Locate and identify every blood parasite.
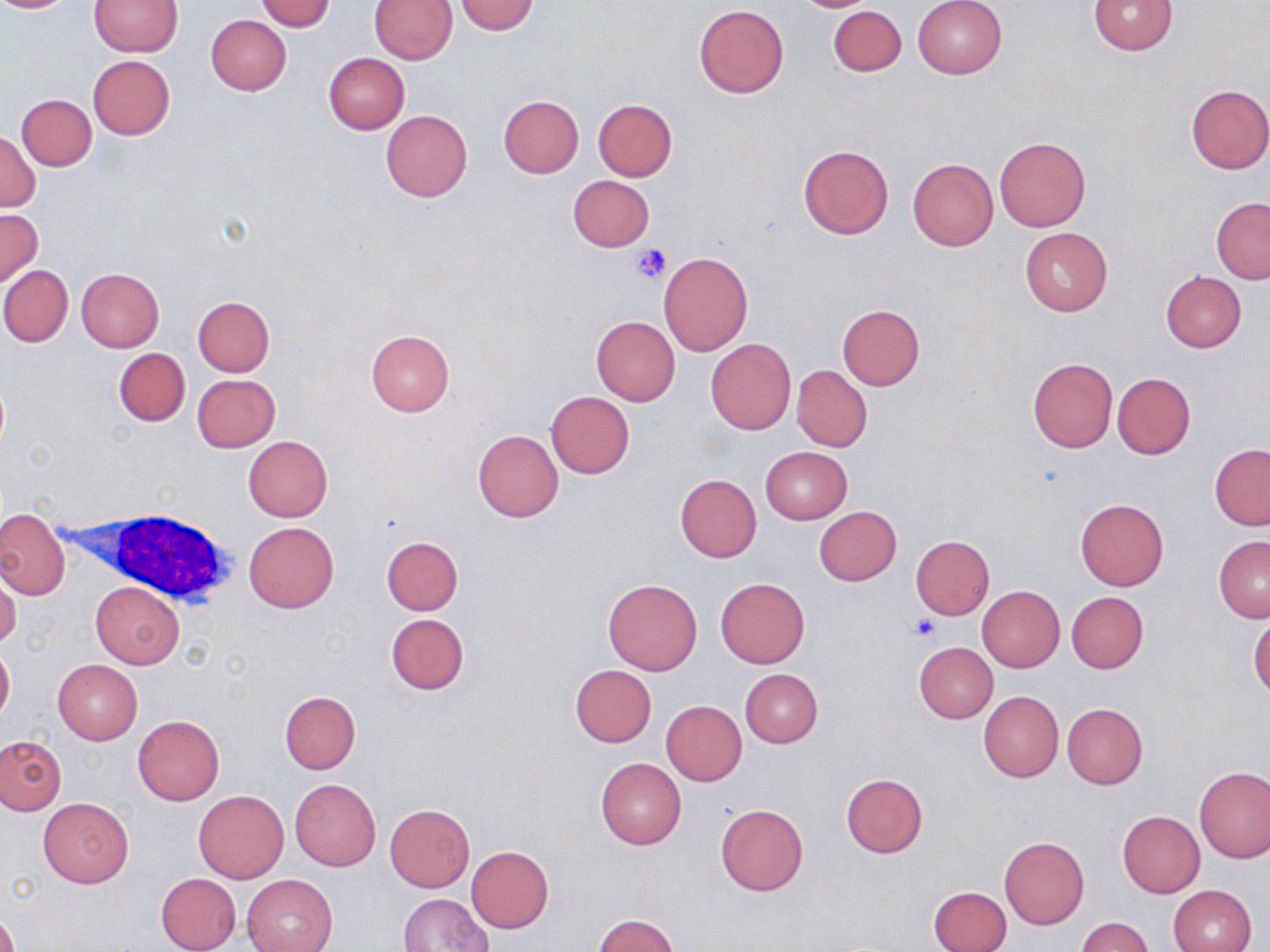

No blood parasites seen.

slide-level diagnosis = no evidence of blood parasites
preparation = thin blood smear
field of view = single
platelet locations = approximate bounding boxes as (x1, y1, x2, y2) in pixels: (631, 243, 670, 285), (908, 615, 940, 643)
magnification = 1000x
white blood cell locations = approximate bounding boxes as (x1, y1, x2, y2) in pixels: (90, 506, 238, 608)
modality = optical microscopy
stain = May-Grünwald-Giemsa
image size = 1270×952 pixels
uninfected red blood cell locations = approximate bounding boxes as (x1, y1, x2, y2) in pixels: (0, 0, 74, 14), (369, 0, 458, 64), (790, 0, 882, 12), (912, 0, 1007, 79), (1087, 0, 1178, 55), (90, 1, 182, 56), (256, 1, 335, 31), (453, 1, 538, 35), (693, 5, 789, 97), (828, 5, 906, 76), (206, 15, 292, 95), (324, 53, 410, 134), (87, 55, 174, 140), (1185, 84, 1270, 175), (18, 93, 97, 170), (498, 96, 584, 178), (593, 99, 677, 180), (380, 111, 472, 201), (0, 129, 41, 212), (994, 137, 1091, 231), (798, 145, 893, 239), (908, 158, 998, 250), (567, 175, 655, 252), (1211, 198, 1270, 284), (0, 209, 42, 286), (1020, 227, 1112, 315), (658, 252, 752, 356), (0, 266, 72, 347), (76, 268, 165, 352), (1160, 271, 1246, 353), (194, 296, 275, 376), (836, 304, 925, 389), (592, 316, 680, 405), (365, 331, 454, 417), (706, 339, 795, 434), (114, 348, 190, 426), (1027, 358, 1118, 453), (791, 365, 872, 452), (1113, 373, 1195, 459), (193, 374, 280, 451), (546, 391, 635, 478), (473, 430, 563, 521), (244, 436, 332, 522), (1210, 443, 1270, 530), (760, 447, 852, 524), (674, 474, 762, 563), (1075, 498, 1169, 590), (814, 506, 902, 586), (0, 509, 68, 598), (243, 522, 338, 612), (382, 535, 463, 614), (910, 535, 994, 620), (1213, 535, 1270, 622), (0, 572, 21, 649), (715, 578, 809, 668), (603, 580, 702, 675), (91, 581, 183, 668), (977, 586, 1065, 672), (1066, 591, 1148, 673), (385, 614, 469, 695), (1248, 614, 1270, 700), (0, 640, 14, 727), (914, 642, 998, 723), (53, 659, 142, 745), (571, 664, 657, 746), (740, 669, 823, 748), (978, 690, 1063, 782), (281, 691, 360, 773), (661, 700, 747, 785), (1062, 703, 1148, 790), (133, 716, 224, 805), (0, 736, 65, 815), (595, 757, 686, 850), (1194, 766, 1269, 863), (840, 773, 928, 858), (290, 779, 381, 871), (194, 791, 288, 883), (39, 798, 134, 887), (384, 804, 475, 891), (715, 804, 808, 896), (1118, 811, 1205, 897), (999, 837, 1089, 929), (467, 845, 554, 933), (155, 872, 240, 951), (243, 874, 337, 952), (1167, 884, 1256, 952), (930, 885, 1012, 952), (400, 893, 492, 952), (0, 904, 19, 952), (595, 914, 678, 952), (1074, 917, 1154, 952)